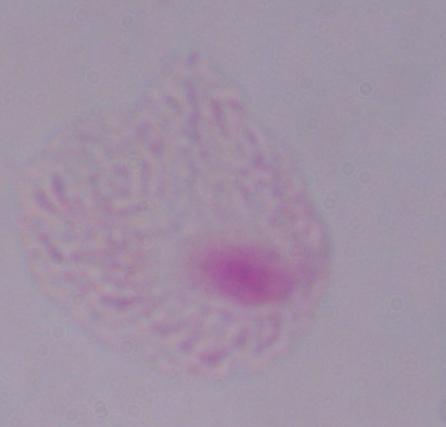

magnification: 1000x
modality: photomicrograph
identification: trichomonad